Assess this cell for malaria.
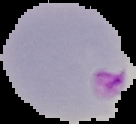

Parasitized.

Summary:
  - Image size: 136×124 pixels
  - Image type: cell region segmented out of the field of view; surrounding area masked to black
  - Preparation: thin blood smear